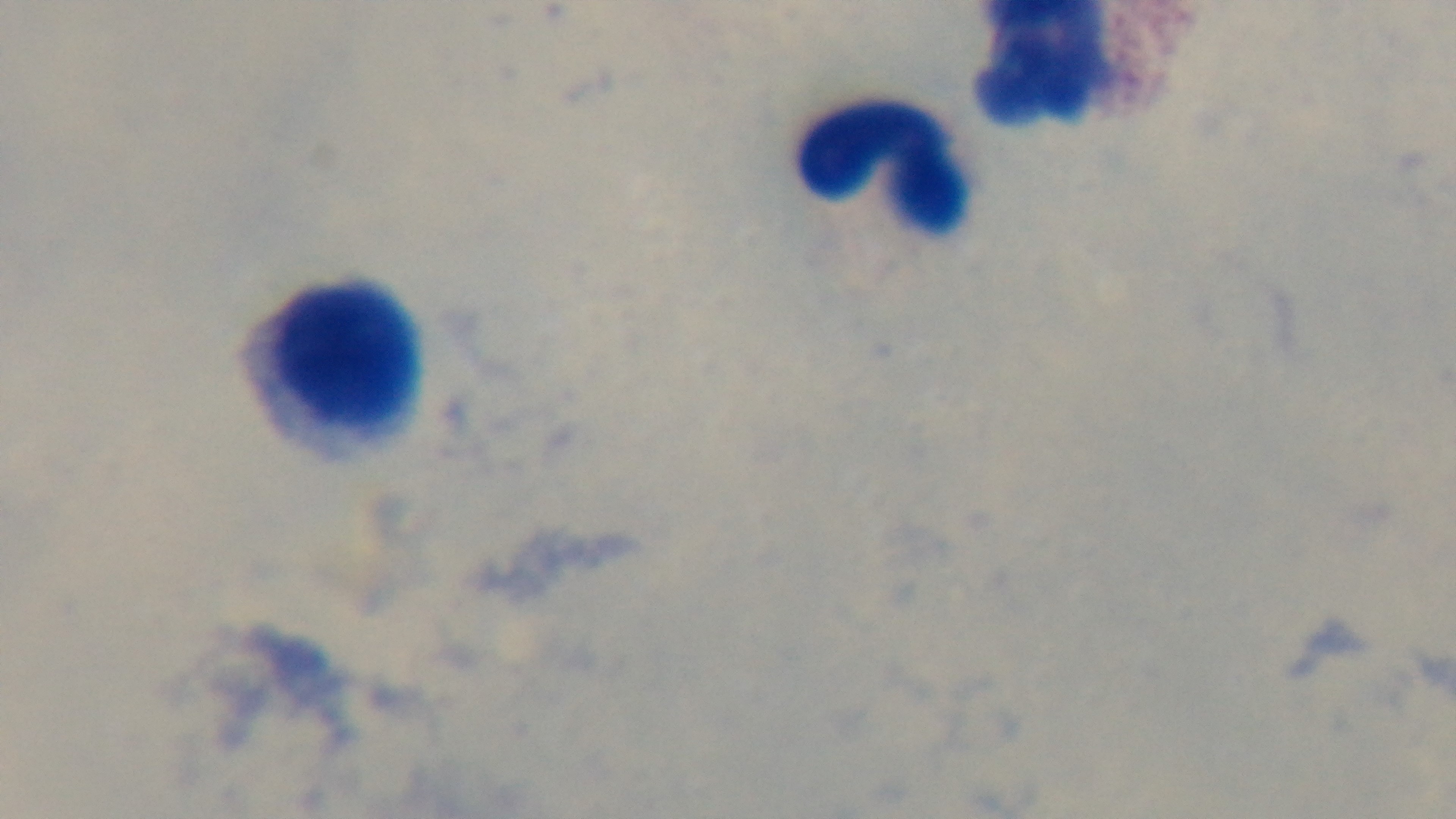

preparation = thick blood film
objective = 100x oil immersion
malaria status = negative
stain = Giemsa
modality = light microscopy
capture = mounted 4K digital camera
field of view = one from the slide